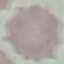 Malaria status: uninfected. Thin blood smear. Photographed with a smartphone camera at the microscope eyepiece. Automatically extracted cell patch, resized to 64 × 64 pixels. Giemsa stain.